Identify the parasite.
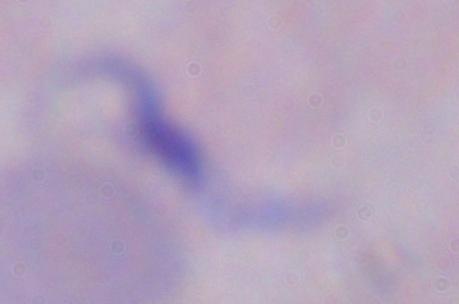

This is a trypanosome.

Micrograph. 1000x magnification.